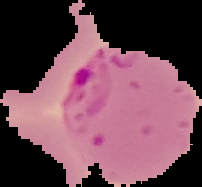

Result: Plasmodium parasites identified. Image is 202×187 pixels. From a thin blood film. Segmented cell region on a black background.